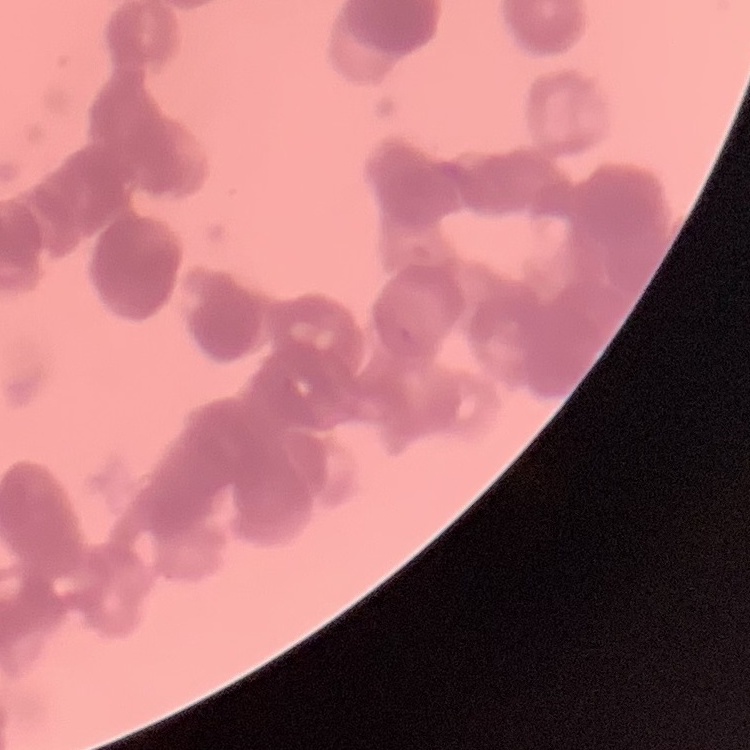

{
  "red_blood_cell_morphology": "rouleaux formation",
  "image_type": "square crop of a larger photomicrograph",
  "preparation": "thin peripheral smear",
  "stain": "Field's or Giemsa"
}